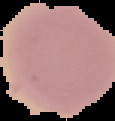
Summary:
  - Result: no malaria parasites seen
  - Image size: 115×121 pixels
  - Image type: cell region segmented out of the field of view; surrounding area masked to black
  - Preparation: thin blood film